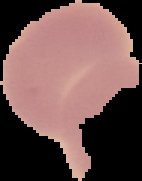

From a thin blood smear. The area outside the segmented cell region is set to black. Image is 142×181 pixels. Result: no malaria parasites detected.